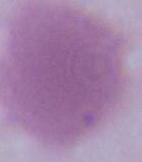
identification: erythrocyte
modality: micrograph
magnification: 1000x